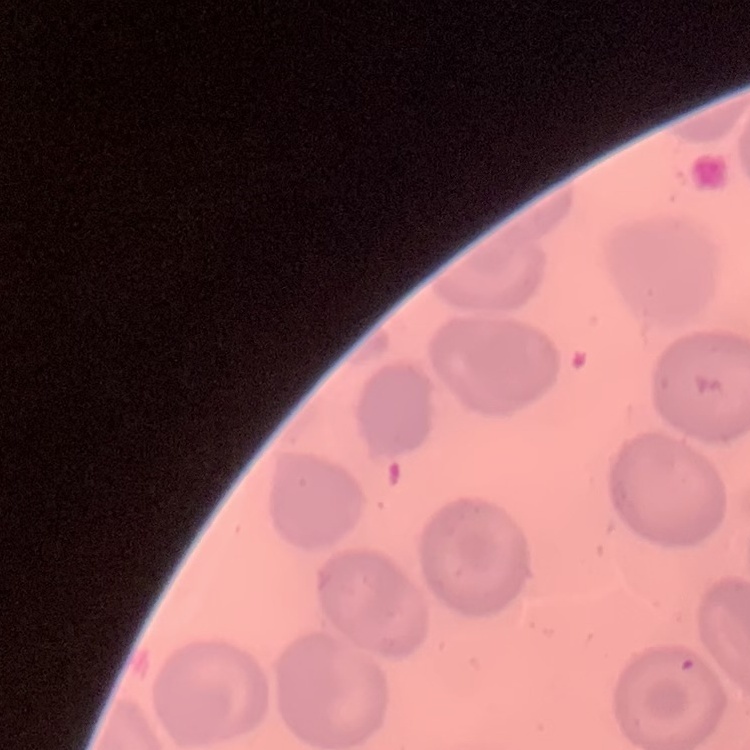

red blood cell morphology = no rouleaux formation
image type = square crop of a larger photomicrograph
stain = Field's or Giemsa
preparation = thin blood smear